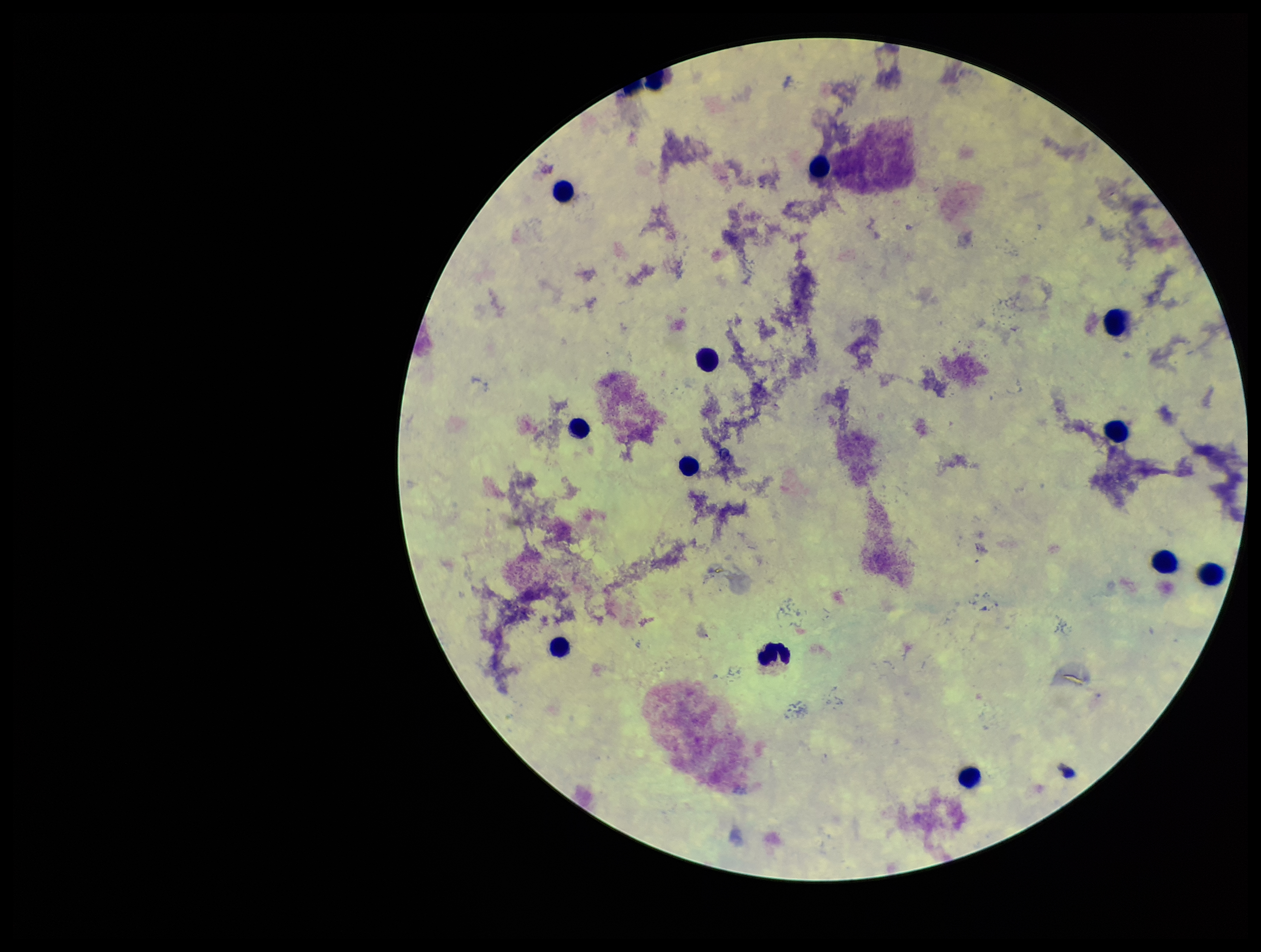

Summary:
  - Capture: smartphone photograph through the microscope eyepiece
  - Parasite count: 0
  - Image size: 1261×952 pixels
  - Patient malaria status: negative
  - Stain: Giemsa
  - Plasmodium parasites: none identified
  - Preparation: thick smear
  - Leukocyte count: 12
  - Field of view: single